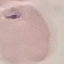

malaria status = parasitized
capture = smartphone through the microscope eyepiece
preparation = thin blood smear
image type = cell patch, automatically extracted from a larger field of view and resized to 64 × 64 pixels
stain = Giemsa